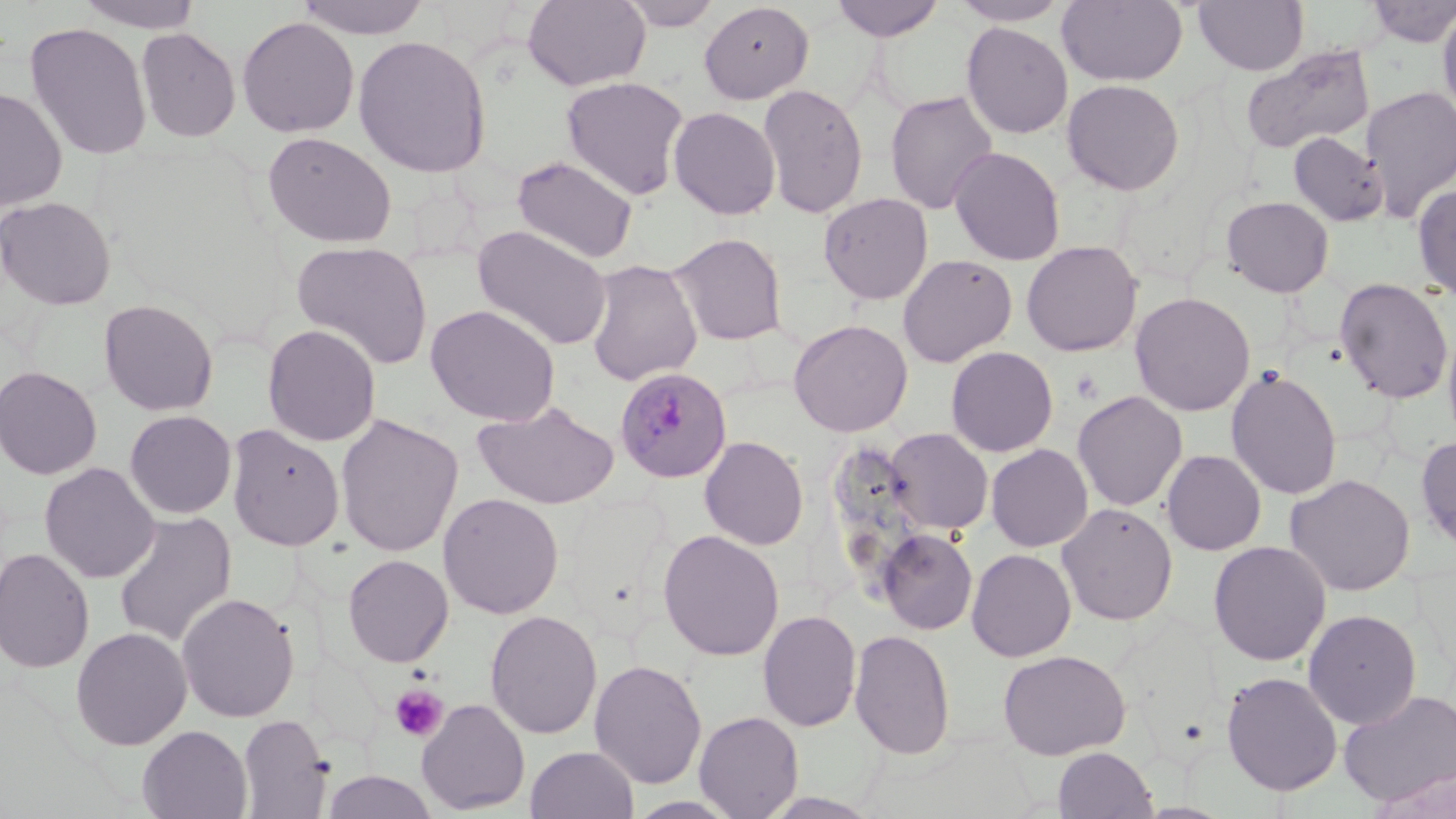

Summary:
  - Coordinate format: approximate bounding boxes as [x1, y1, x2, y2] in pixels
  - Plasmodium malariae-infected red blood cell locations: [614, 366, 732, 484]
  - Platelet locations: [390, 684, 449, 742]
  - Uninfected red blood cell locations: [75, 0, 206, 33], [293, 0, 433, 39], [522, 0, 651, 91], [618, 0, 722, 30], [829, 0, 947, 41], [950, 0, 1070, 26], [1057, 0, 1188, 87], [1194, 0, 1309, 75], [1362, 0, 1456, 47], [699, 2, 814, 104], [1437, 3, 1456, 124], [237, 16, 359, 138], [24, 22, 153, 161], [961, 22, 1073, 139], [135, 27, 241, 143], [352, 34, 492, 178], [1240, 44, 1376, 154], [561, 76, 689, 199], [1061, 79, 1185, 196], [758, 83, 868, 219], [1360, 84, 1456, 221], [0, 85, 67, 212], [884, 90, 999, 214], [668, 106, 781, 220], [262, 131, 397, 248], [1288, 132, 1389, 227], [948, 146, 1066, 266], [511, 155, 639, 264], [1412, 183, 1456, 303], [819, 192, 933, 305], [1221, 195, 1335, 297], [0, 196, 116, 310], [472, 224, 612, 352], [668, 232, 789, 346], [1021, 240, 1143, 357], [291, 241, 434, 371], [898, 254, 1017, 367], [585, 259, 703, 386], [1334, 277, 1454, 404], [1130, 291, 1255, 417], [98, 299, 218, 416], [425, 304, 560, 427], [788, 318, 913, 437], [1442, 320, 1456, 451], [262, 324, 381, 446], [946, 346, 1058, 457], [0, 366, 102, 480], [1226, 367, 1342, 500], [1072, 390, 1188, 512], [472, 400, 620, 510], [124, 410, 237, 519], [336, 413, 464, 557], [226, 423, 345, 551], [884, 427, 993, 536], [700, 435, 809, 550], [1416, 435, 1456, 555], [986, 443, 1093, 551], [1161, 449, 1267, 556], [39, 462, 161, 584], [1285, 473, 1415, 596], [438, 492, 564, 619], [1056, 502, 1178, 625], [113, 512, 237, 648], [877, 528, 978, 635], [658, 529, 785, 661], [1208, 540, 1331, 666], [0, 547, 95, 673], [966, 548, 1077, 661], [342, 553, 454, 668], [176, 592, 300, 723], [758, 609, 861, 732], [484, 610, 602, 740], [1303, 610, 1422, 730], [70, 626, 192, 750], [850, 628, 956, 760], [998, 649, 1130, 760], [589, 658, 707, 789], [1221, 671, 1343, 797], [1338, 689, 1456, 807], [417, 698, 530, 814], [694, 710, 804, 818], [237, 714, 333, 818], [137, 725, 252, 819], [525, 745, 639, 819], [1053, 746, 1158, 819], [1368, 767, 1456, 818], [321, 771, 438, 819], [626, 795, 744, 818]
  - Slide-level diagnosis: Plasmodium malariae
  - Modality: light microscopy
  - Image size: 1456×819 pixels
  - Stain: May-Grünwald-Giemsa
  - Field of view: single
  - Preparation: thin blood film
  - Magnification: 1000x